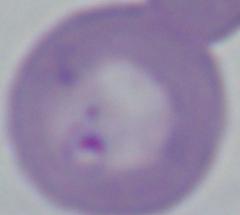

Summary:
  - Modality: photomicrograph
  - Identification: Babesia
  - Magnification: 1000x